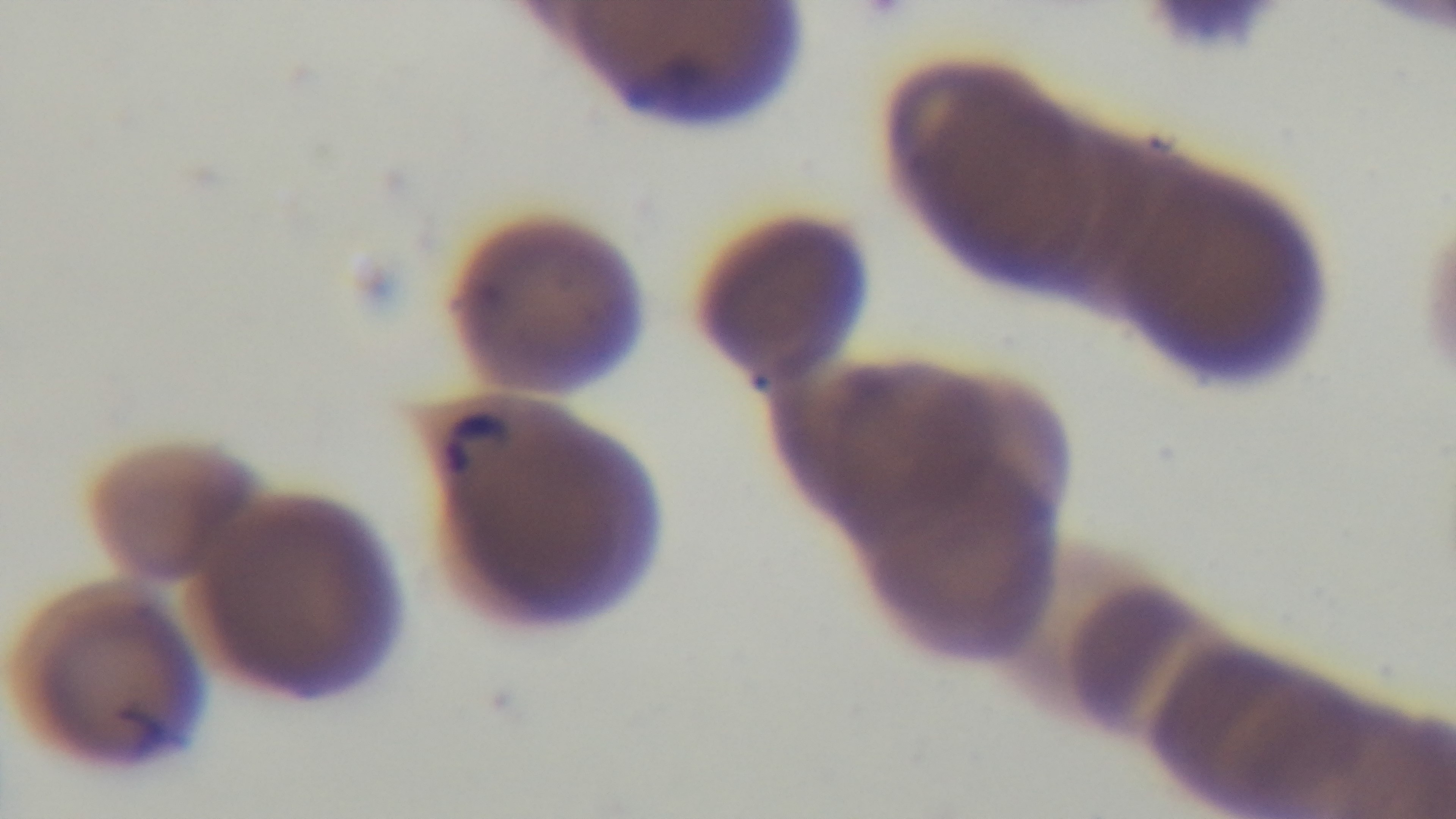 Giemsa stain. Light microscopy. 100x oil-immersion objective. Mounted 4K digital camera. Single field of view. Preparation: thin. Malaria status: positive.